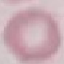 Malaria status: uninfected. Cell patch, automatically extracted from a larger field of view and resized to 64 × 64 pixels. Giemsa-stained preparation. Thin blood film. Acquired by smartphone through the microscope eyepiece.